Name the cell type shown.
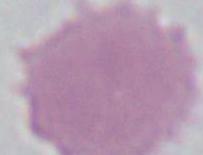

An erythrocyte.

modality: photomicrograph
magnification: 1000x